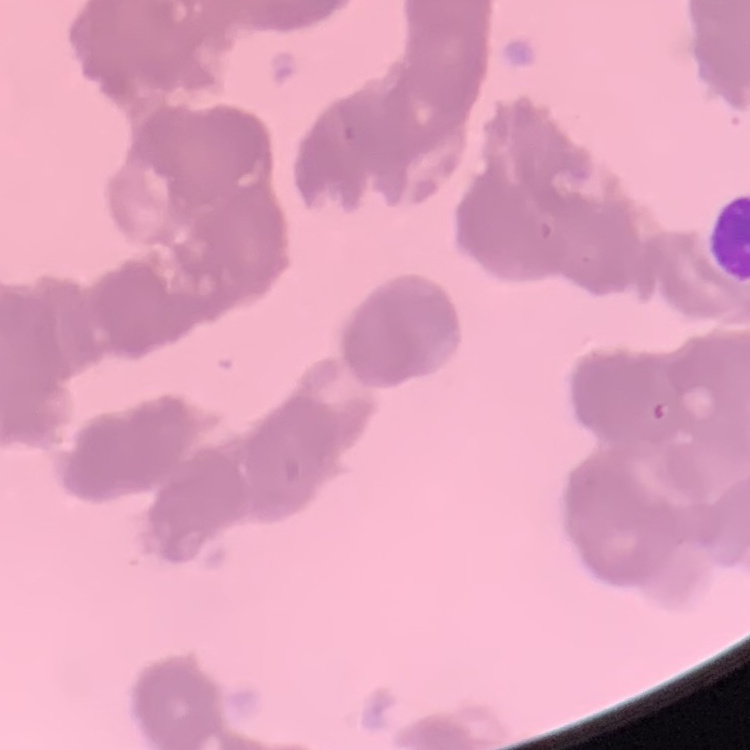 The red blood cells exhibit rouleaux formation. One tile cut from a larger photomicrograph. Thin blood film. Stained with either Field's or Giemsa.